Assess this cell for malaria.
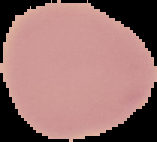

It is uninfected.

image type = cell region segmented out of the field of view; surrounding area masked to black
preparation = thin blood smear
image size = 157×142 pixels